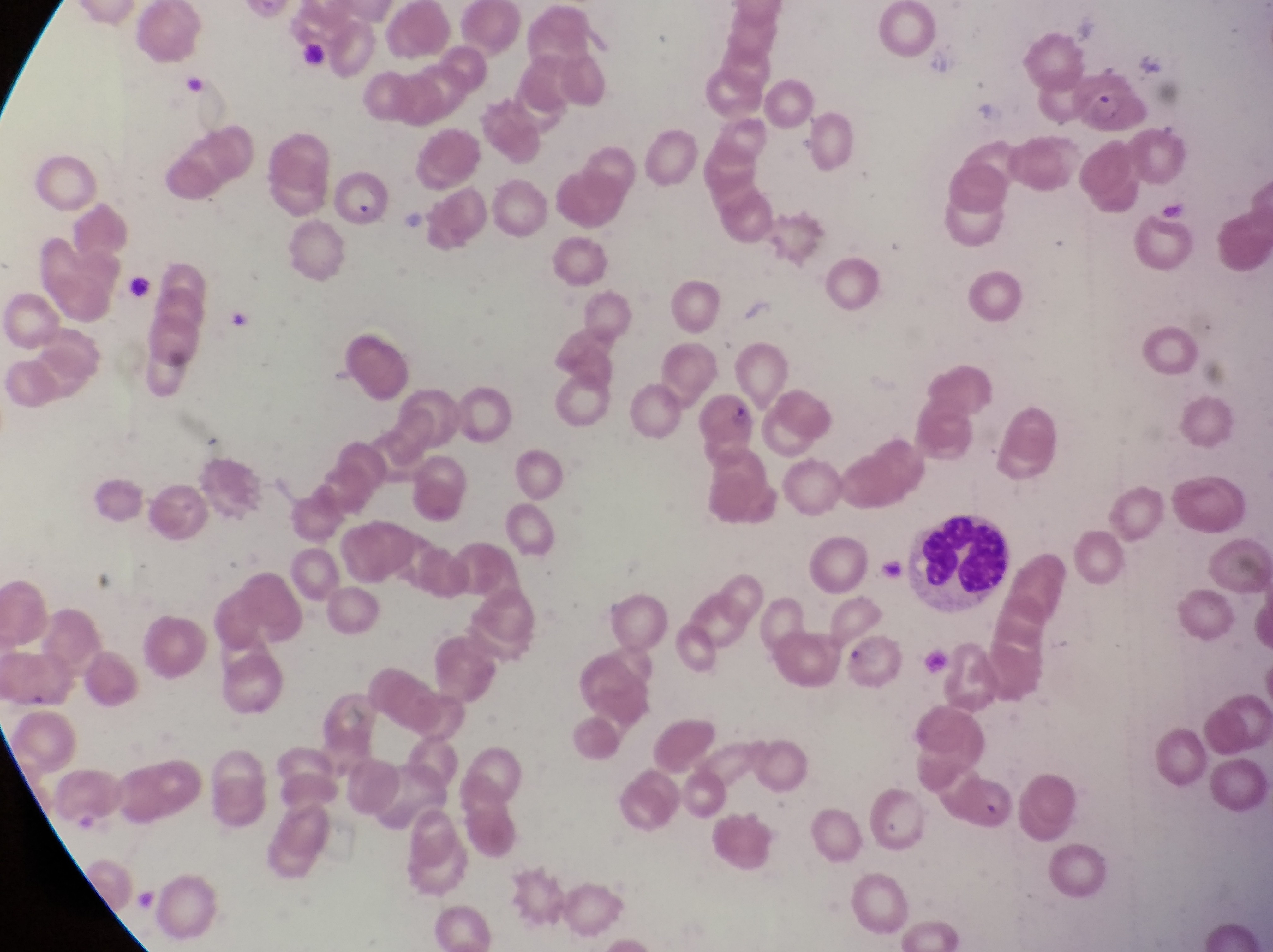

image_size: 1273×952 pixels
capture: smartphone photograph through the eyepiece of an Olympus CX-23 microscope
leukocyte_locations: 'approximate bounding boxes as {left, top, right, bottom} in pixels: {904, 517, 1008, 610}'
preparation: thin blood film
country: Uganda
magnification: 1000x
parasitised_red_blood_cell_locations: 'approximate bounding boxes as {left, top, right, bottom} in pixels: {1063, 68, 1138, 136}'
field_of_view: single